Point out each malaria parasite.
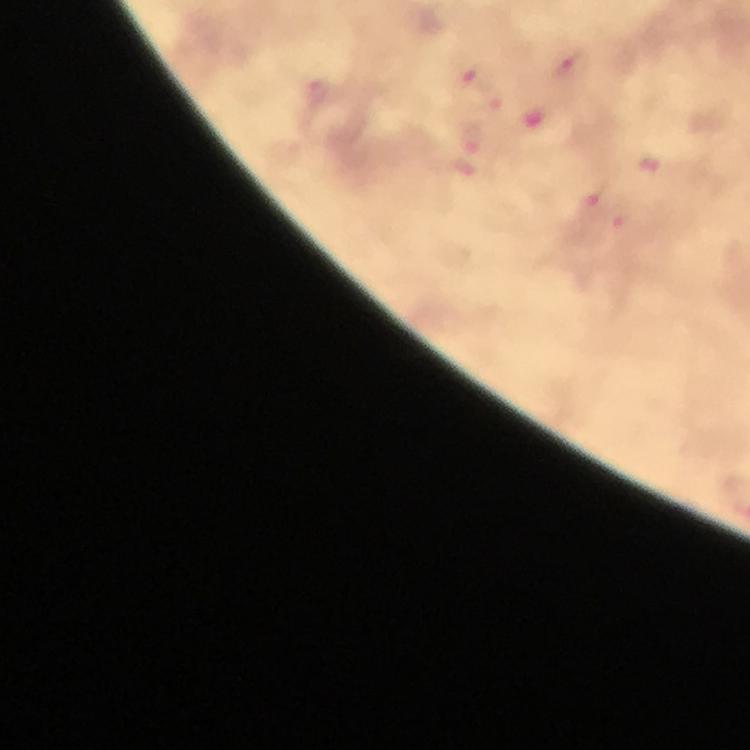
Approximate object centers, in pixels from the top-left corner.
Malaria parasites: (x=573, y=65), (x=478, y=77), (x=318, y=92), (x=471, y=138), (x=606, y=210).

Thick smear. Smartphone photograph taken through a microscope. 100x magnification. From a diagnostic examination for malaria. Immersion oil applied. Cropped region of a single field of view. Giemsa-stained preparation. Image is 750×750 pixels.